Locate every parasitized red blood cell.
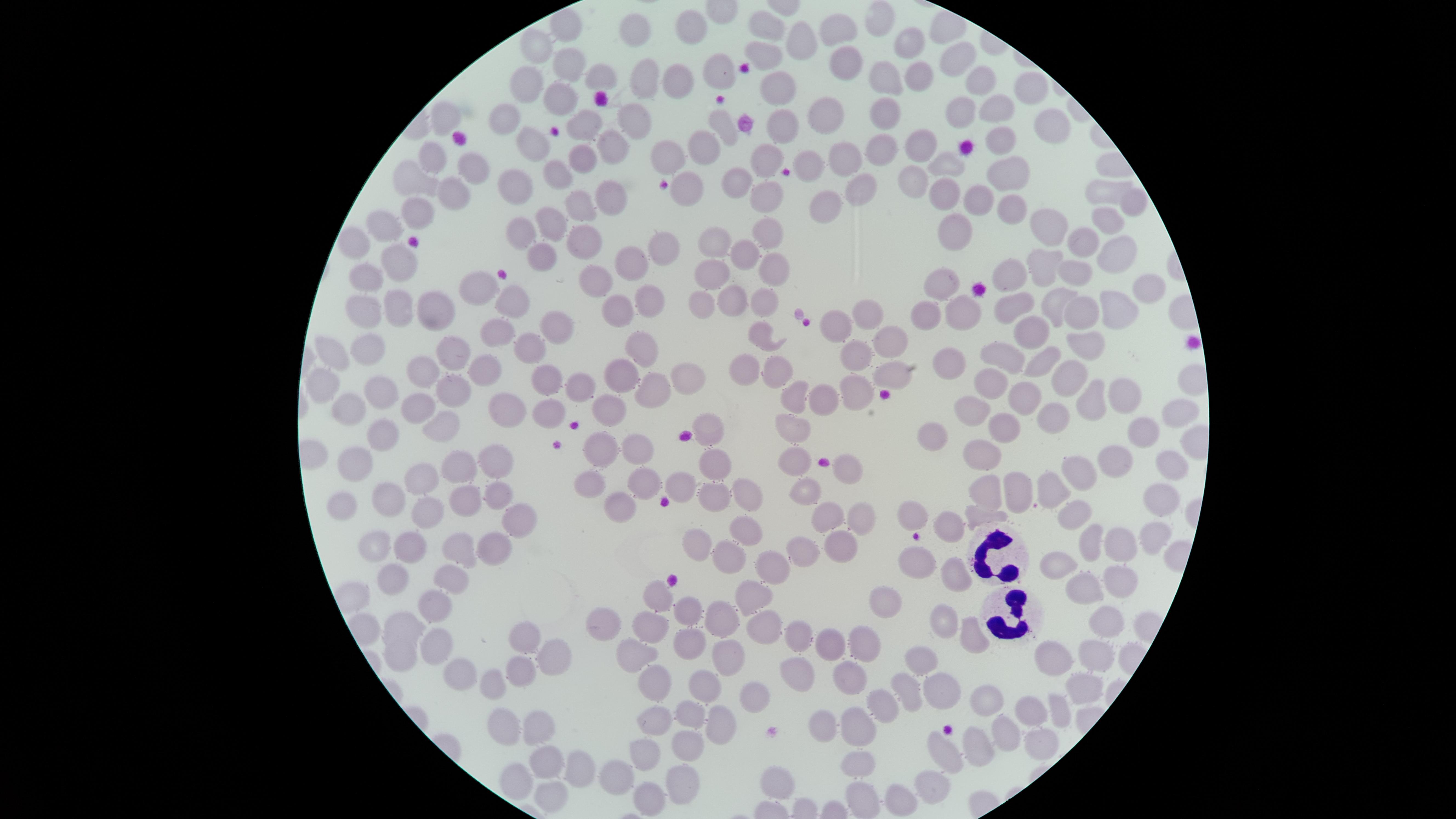
No parasitized red blood cells identified.

Approximate marker points as [x, y] in pixels.
Summary:
  - White blood cells: [996, 555], [1011, 613]
  - Uninfected red blood cells: [880, 18], [569, 23], [693, 26], [769, 27], [837, 29], [636, 32], [913, 39], [802, 43], [541, 45], [767, 52], [837, 60], [959, 61], [568, 64], [718, 68], [602, 74], [915, 75], [880, 76], [530, 81], [678, 82], [979, 83], [645, 85], [1033, 87], [779, 89], [559, 96], [886, 107], [995, 110], [956, 112], [824, 114], [508, 117], [454, 120], [633, 120], [783, 122], [719, 123], [587, 125], [1050, 125], [1003, 137], [535, 141], [921, 141], [880, 142], [615, 143], [699, 143], [434, 155], [665, 155], [847, 155], [587, 160], [951, 160], [769, 161], [812, 168], [474, 169], [562, 172], [411, 175], [1007, 175], [911, 178], [741, 179], [518, 181], [1103, 187], [690, 188], [857, 189], [764, 190], [941, 192], [452, 195], [614, 195], [973, 200], [588, 204], [1132, 204], [417, 205], [822, 206], [1008, 210], [557, 222], [1102, 222], [1046, 223], [955, 227], [387, 228], [516, 228], [769, 232], [1084, 238], [716, 240], [356, 241], [580, 241], [659, 248], [749, 251], [533, 254], [1117, 254], [631, 262], [400, 263], [1045, 264], [774, 265], [712, 271], [1014, 271], [1072, 274], [368, 276], [600, 277], [946, 280], [475, 287], [1151, 289], [729, 294], [760, 296], [650, 297], [508, 298], [1053, 299], [400, 300], [701, 301], [1017, 304], [371, 307], [430, 307], [961, 307], [1083, 308], [1120, 311], [871, 312], [925, 312], [619, 314], [552, 326], [832, 327], [1028, 327], [493, 333], [762, 333], [645, 341], [1082, 341], [890, 344], [371, 347], [337, 351], [523, 351], [456, 353], [1002, 354], [858, 355], [1044, 358], [950, 361], [745, 365], [479, 370], [783, 370], [626, 373], [688, 373], [419, 374], [891, 375], [545, 376], [1070, 376], [323, 380], [989, 380], [859, 385], [581, 387], [379, 390], [653, 390], [454, 391], [1122, 392], [793, 394], [822, 395], [1024, 395], [1093, 401], [346, 405], [419, 405], [552, 406], [1176, 406], [615, 408], [974, 408], [506, 409], [1051, 414], [1010, 420], [445, 425], [793, 427], [712, 428], [930, 430], [1143, 430], [380, 431], [640, 446], [605, 449], [980, 449], [360, 456], [1121, 457], [496, 462], [798, 462], [716, 463], [460, 466], [847, 467], [1163, 470], [1087, 472], [427, 477], [645, 479], [683, 483], [1048, 485], [592, 487], [984, 488], [1014, 489], [746, 491], [809, 492], [395, 494], [494, 494], [1155, 496], [351, 498], [713, 499], [462, 500], [427, 507], [621, 508], [913, 514], [518, 516], [827, 517], [977, 517], [1081, 517], [863, 522], [955, 524], [747, 530], [1145, 532], [1092, 537], [1120, 541], [377, 542], [415, 542], [696, 543], [499, 545], [456, 547], [846, 547], [803, 555], [726, 560], [916, 562], [1055, 564], [779, 570], [957, 575], [395, 577], [449, 578], [1114, 582], [1075, 587], [756, 596], [662, 598], [435, 600], [886, 600], [688, 611], [941, 617], [1102, 617], [401, 619], [717, 619], [610, 621], [770, 624], [651, 627], [518, 634], [797, 634], [862, 638], [827, 640], [974, 641], [443, 644], [690, 647], [1098, 650], [1053, 651], [635, 654], [402, 656], [923, 656], [733, 657], [558, 659], [462, 670], [523, 671], [852, 673], [800, 675], [496, 681], [659, 681], [706, 687], [909, 690], [940, 690], [1082, 691], [992, 698], [756, 699], [884, 706], [1028, 708], [1053, 709], [685, 714], [654, 716], [505, 719], [719, 720], [855, 725], [822, 727], [536, 729], [1003, 732], [1038, 744], [686, 745], [973, 748], [946, 752], [645, 754], [543, 760], [857, 760], [576, 766], [615, 775], [518, 781], [779, 783], [931, 784], [685, 785], [555, 795], [904, 796], [648, 798], [862, 799]
  - Capture: smartphone photograph through the microscope eyepiece
  - Visible region: circular
  - Field of view: single
  - Stain: Giemsa
  - Image size: 1456×819 pixels
  - Preparation: thin smear of blood